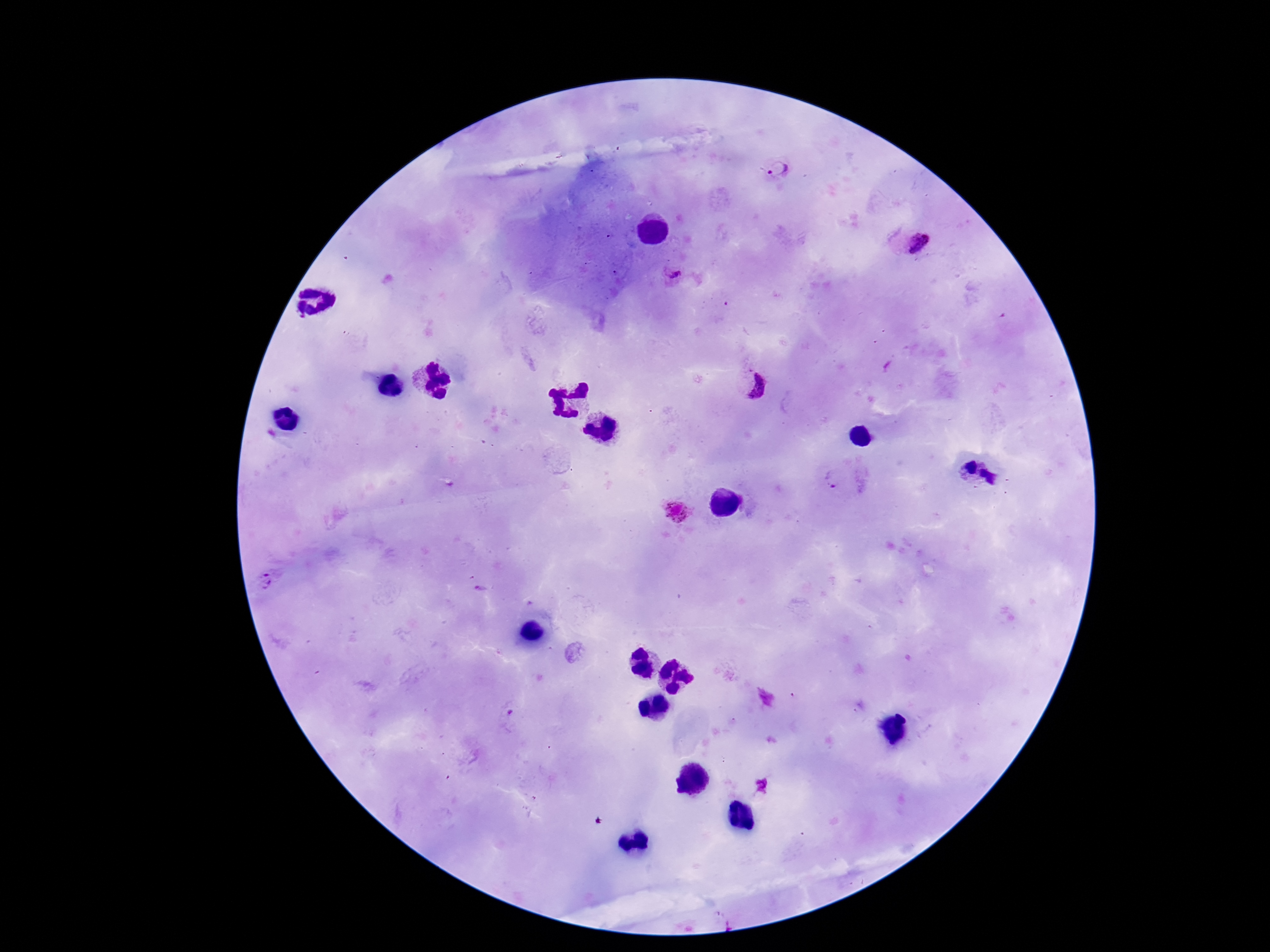

Approximate object centers, in pixels from the top-left corner.
Summary:
  - Plasmodium parasite locations: (x=778, y=170), (x=910, y=242), (x=675, y=276), (x=752, y=385), (x=834, y=479), (x=674, y=512), (x=266, y=581), (x=481, y=588), (x=511, y=712)
  - Capture: smartphone camera through the microscope eyepiece
  - Patient malaria status: infected
  - Field of view: single
  - Stain: Giemsa
  - Image size: 1270×952 pixels
  - Magnification: 100x
  - Preparation: thick blood film